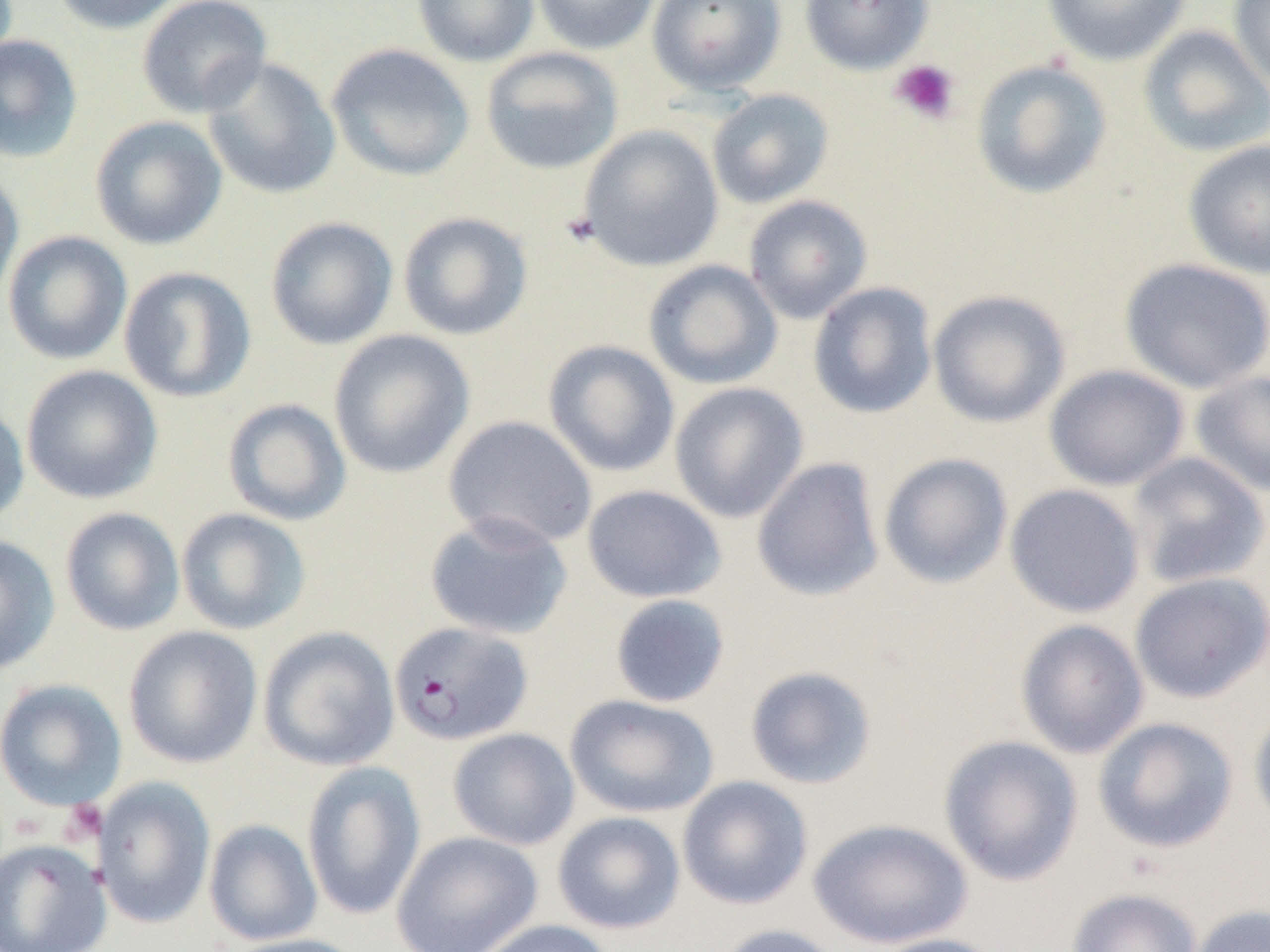
slide_level_diagnosis: Plasmodium falciparum
modality: optical microscopy
image_size: 1270×952 pixels
platelet_locations: 'approximate bounding boxes as [x1, y1, x2, y2] in pixels: [890, 59, 960, 124], [61, 799, 108, 844]'
magnification: 1000x
field_of_view: one of a larger specimen
plasmodium_falciparum_infected_red_blood_cell_locations: 'approximate bounding boxes as [x1, y1, x2, y2] in pixels: [389, 621, 534, 746]'
preparation: thin blood film
uninfected_red_blood_cell_locations: 'approximate bounding boxes as [x1, y1, x2, y2] in pixels: [51, 0, 186, 35], [136, 0, 273, 119], [412, 0, 540, 67], [531, 0, 661, 55], [646, 0, 786, 96], [799, 0, 935, 74], [1041, 0, 1191, 66], [1228, 0, 1270, 92], [1138, 24, 1270, 158], [0, 34, 83, 163], [326, 43, 475, 181], [480, 46, 624, 175], [202, 56, 342, 200], [971, 59, 1113, 199], [707, 89, 834, 209], [89, 115, 228, 250], [577, 125, 724, 272], [1183, 139, 1270, 279], [0, 168, 24, 307], [743, 195, 873, 325], [397, 211, 533, 340], [265, 216, 398, 350], [2, 231, 133, 365], [1120, 258, 1270, 394], [642, 259, 783, 390], [118, 266, 257, 403], [808, 282, 938, 419], [927, 289, 1071, 428], [328, 329, 475, 479], [543, 339, 680, 477], [21, 364, 163, 504], [1043, 364, 1189, 491], [1190, 370, 1270, 497], [669, 382, 808, 523], [222, 398, 351, 526], [0, 400, 29, 529], [443, 415, 598, 550], [878, 452, 1013, 588], [1126, 452, 1269, 589], [751, 457, 885, 602], [1004, 483, 1145, 618], [582, 484, 727, 603], [60, 507, 185, 636], [176, 508, 311, 635], [424, 511, 573, 640], [0, 534, 60, 675], [1129, 572, 1270, 704], [609, 594, 731, 708], [1015, 619, 1149, 759], [123, 624, 263, 769], [258, 626, 400, 772], [744, 665, 878, 789], [0, 678, 127, 811], [564, 694, 719, 818], [1248, 704, 1270, 832], [1092, 717, 1239, 854], [447, 727, 580, 850], [938, 734, 1083, 886], [302, 760, 426, 921], [677, 775, 813, 910], [93, 776, 216, 929], [552, 811, 686, 934], [809, 817, 973, 950], [204, 819, 322, 946], [391, 830, 544, 952], [0, 838, 111, 951], [1066, 888, 1203, 952], [1189, 904, 1270, 952], [471, 918, 617, 952], [715, 923, 847, 952], [867, 932, 1009, 952], [222, 933, 367, 952]'